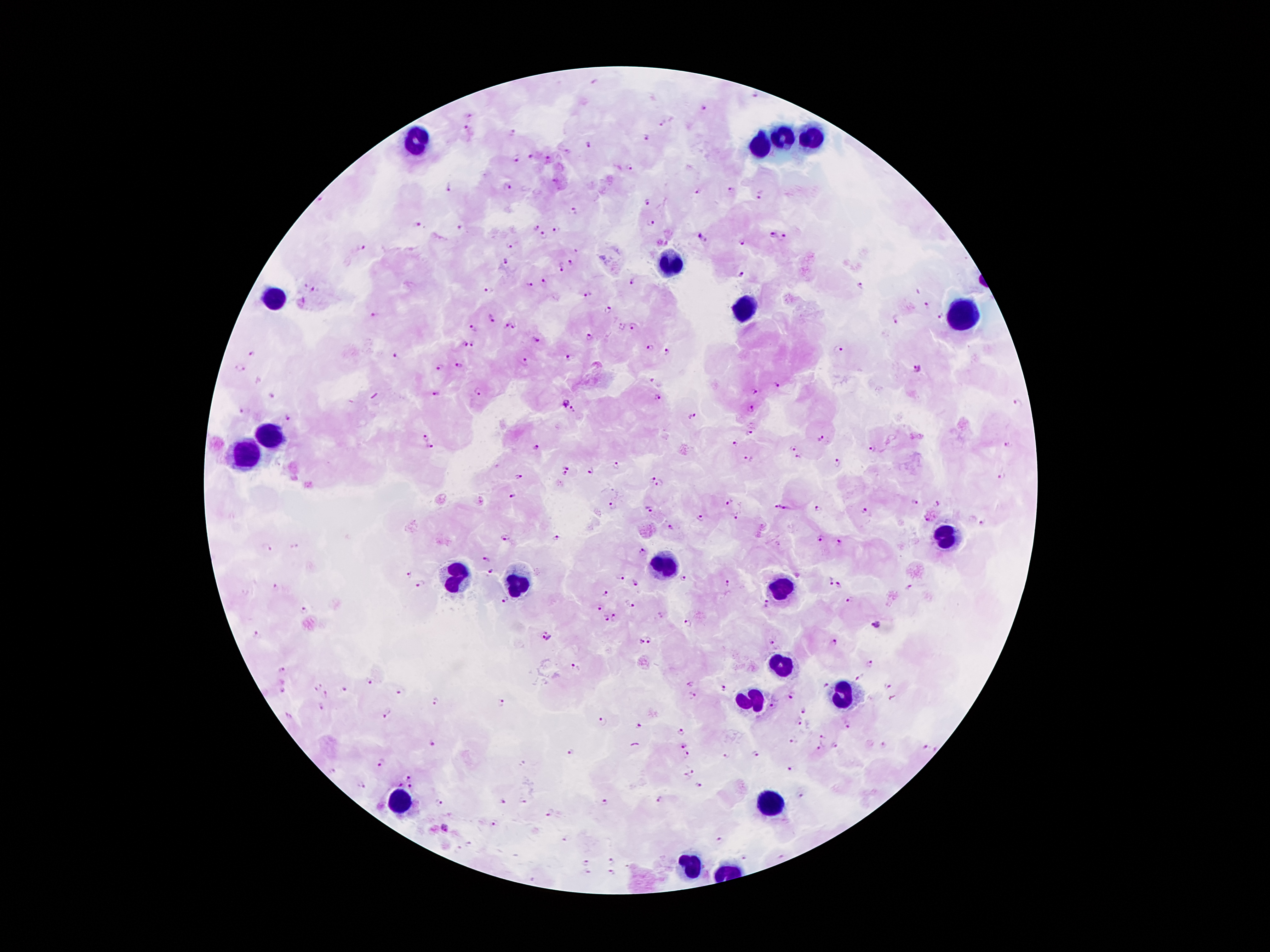 Patient malaria status: positive for Plasmodium falciparum. Thick blood film. Giemsa-stained preparation. Single field of view. Photographed through the microscope eyepiece with a smartphone camera. 100x magnification. Image is 1270×952 pixels.